Report the malaria status of this cell.
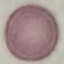

It is uninfected.

Summary:
  - Capture: smartphone through the microscope eyepiece
  - Stain: Giemsa
  - Preparation: thin blood film
  - Image type: cell patch, automatically extracted from a larger field of view and resized to 64 × 64 pixels